Locate and identify every blood parasite.
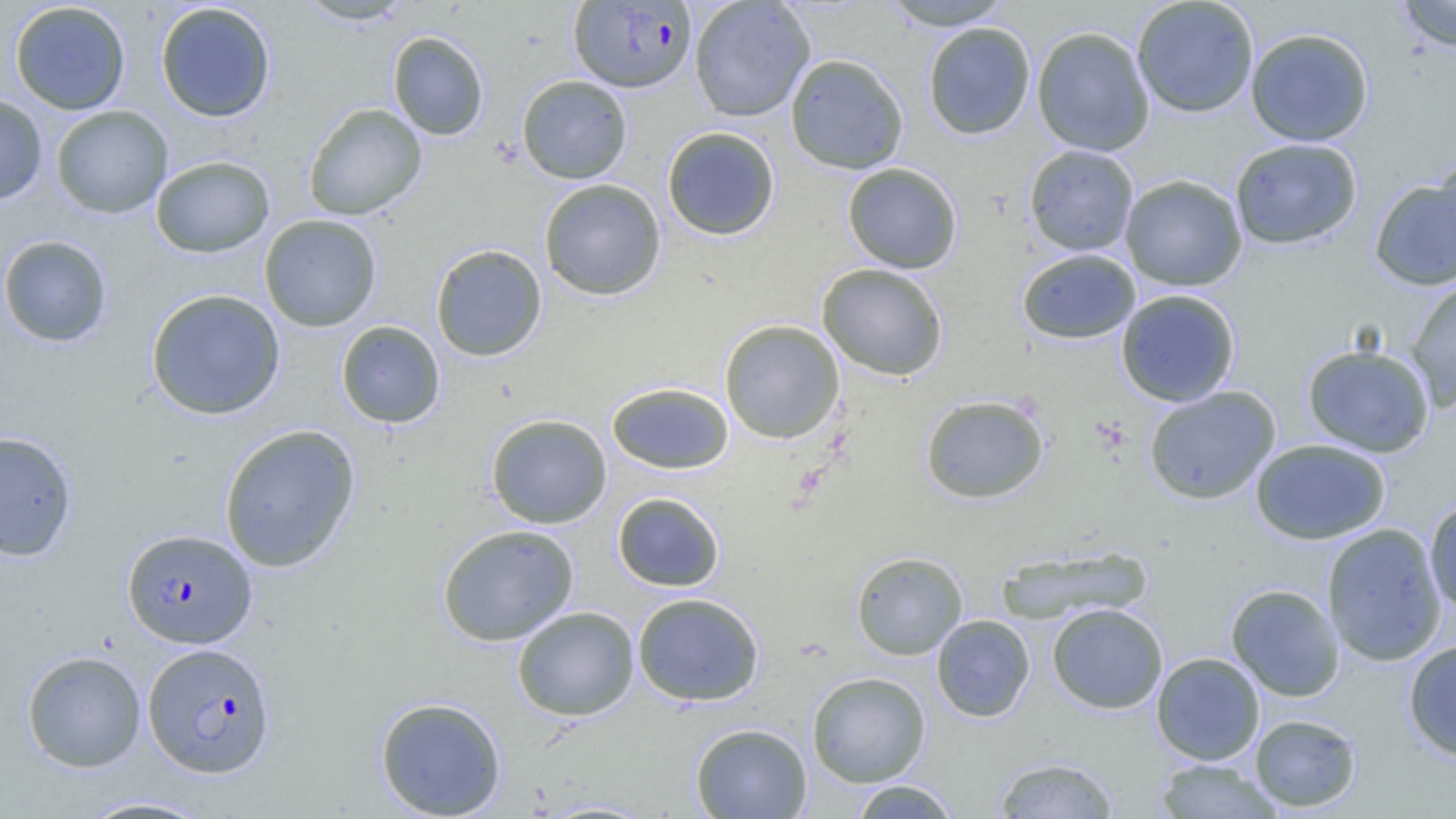

Approximate bounding boxes as (x1, y1, x2, y2) in pixels.
Plasmodium falciparum-infected red blood cells: (569, 1, 696, 92), (122, 528, 258, 649), (142, 642, 275, 778).
No Plasmodium ovale, Plasmodium malariae, Plasmodium vivax, Babesia divergens, or Trypanosoma brucei observed.

Uninfected red blood cell locations: (295, 0, 415, 26), (689, 0, 815, 122), (880, 0, 1015, 31), (1131, 0, 1260, 117), (1395, 0, 1456, 53), (10, 2, 131, 115), (155, 2, 276, 123), (923, 22, 1036, 140), (1031, 26, 1155, 156), (1245, 27, 1374, 146), (387, 31, 489, 141), (785, 53, 909, 174), (516, 75, 632, 184), (0, 93, 48, 206), (303, 102, 427, 220), (51, 105, 173, 219), (662, 126, 780, 241), (1228, 138, 1363, 250), (1024, 144, 1139, 256), (1432, 153, 1456, 268), (150, 155, 275, 258), (842, 162, 963, 274), (1120, 174, 1247, 291), (1369, 177, 1456, 290), (538, 178, 666, 301), (259, 214, 382, 332), (0, 234, 113, 348), (430, 244, 547, 362), (1016, 248, 1141, 344), (817, 263, 948, 380), (1404, 276, 1456, 411), (146, 288, 286, 420), (1115, 289, 1241, 407), (719, 319, 845, 444), (336, 320, 446, 428), (1302, 344, 1436, 457), (606, 381, 734, 475), (1143, 386, 1281, 505), (919, 394, 1050, 504), (485, 413, 612, 529), (218, 423, 361, 572), (0, 431, 78, 562), (1250, 438, 1391, 545), (612, 492, 725, 591), (1424, 496, 1456, 616), (1321, 523, 1448, 667), (436, 524, 579, 646), (996, 545, 1152, 626), (850, 551, 968, 660), (1226, 584, 1345, 701), (632, 592, 764, 706), (1046, 603, 1168, 714), (512, 606, 640, 721), (931, 615, 1035, 722), (1403, 639, 1456, 760), (21, 650, 147, 773), (1151, 652, 1265, 765), (807, 671, 931, 787), (374, 696, 507, 818), (1249, 713, 1363, 813), (690, 723, 812, 818), (993, 756, 1120, 818), (1153, 758, 1283, 818), (847, 779, 962, 818), (75, 795, 220, 818), (531, 799, 662, 818). Slide-level diagnosis: Plasmodium falciparum. Thin blood film. Optical microscopy. Captured at 1000x magnification. One field of a larger specimen. Image is 1456×819 pixels.